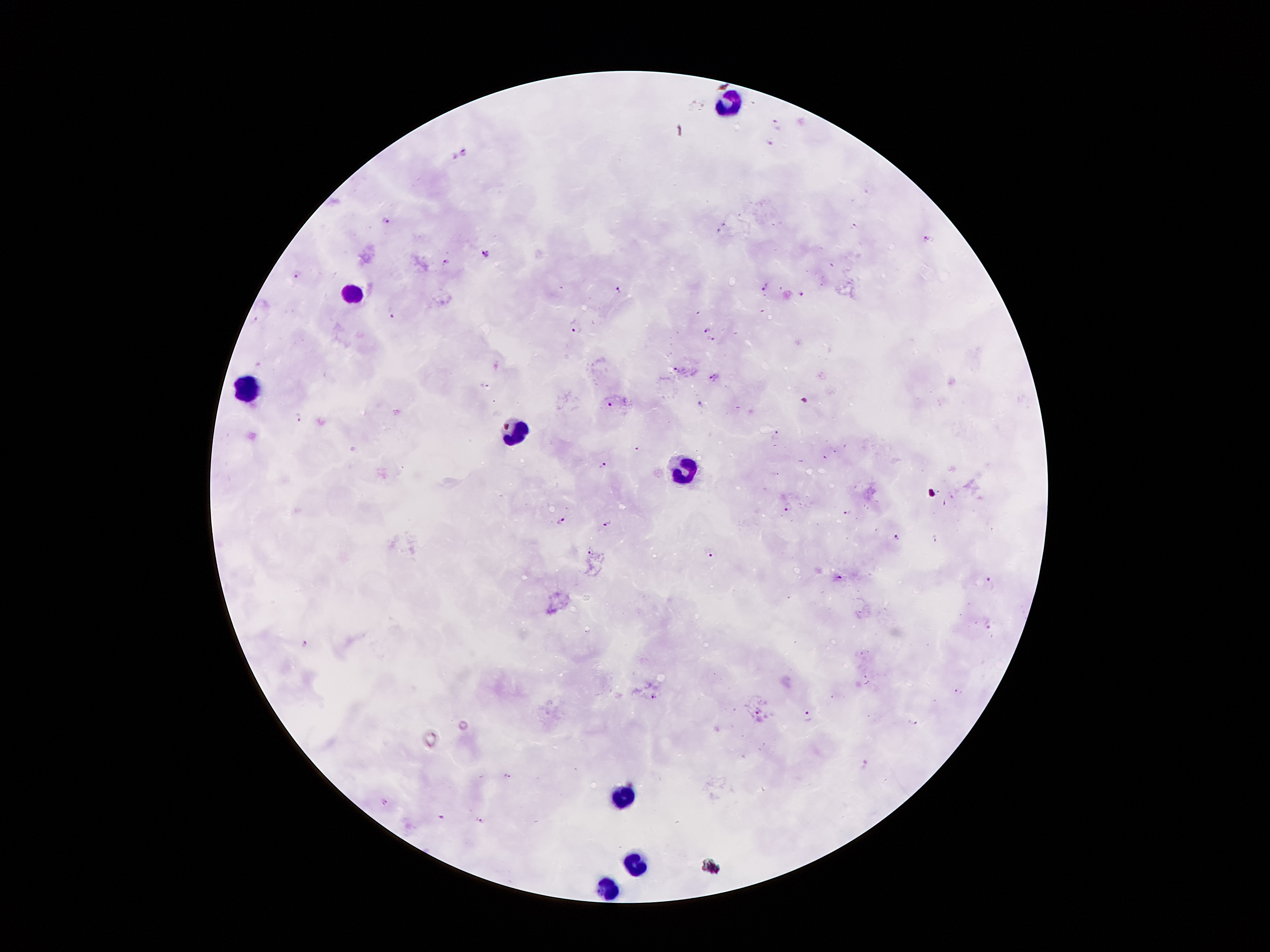 Approximate centers as [x, y] in pixels. Plasmodium parasite locations: [778, 124], [770, 143], [464, 152], [456, 157], [386, 218], [856, 226], [721, 231], [927, 238], [486, 254], [447, 261], [299, 271], [764, 288], [618, 289], [801, 293], [391, 313], [255, 320], [577, 328], [707, 328], [711, 340], [676, 370], [713, 377], [484, 385], [805, 401], [611, 404], [702, 405], [296, 416], [777, 433], [639, 449], [603, 465], [938, 491], [945, 504], [788, 505], [846, 512], [561, 520], [607, 523], [897, 537], [935, 539], [591, 550], [712, 554], [839, 576], [989, 579], [587, 632], [306, 647], [956, 690], [653, 695], [758, 711], [808, 714], [916, 723], [866, 765], [507, 776], [385, 801], [442, 817], [481, 818]. Leukocyte locations: [722, 102], [352, 290], [248, 391], [512, 435], [685, 473], [624, 796], [636, 863], [606, 890]. Image is 1270×952 pixels. Giemsa stain. Patient malaria status: infected with Plasmodium falciparum. Thick blood film. Smartphone photograph taken through the microscope eyepiece. One field from this slide. 100x magnification.